Mark where platelets are.
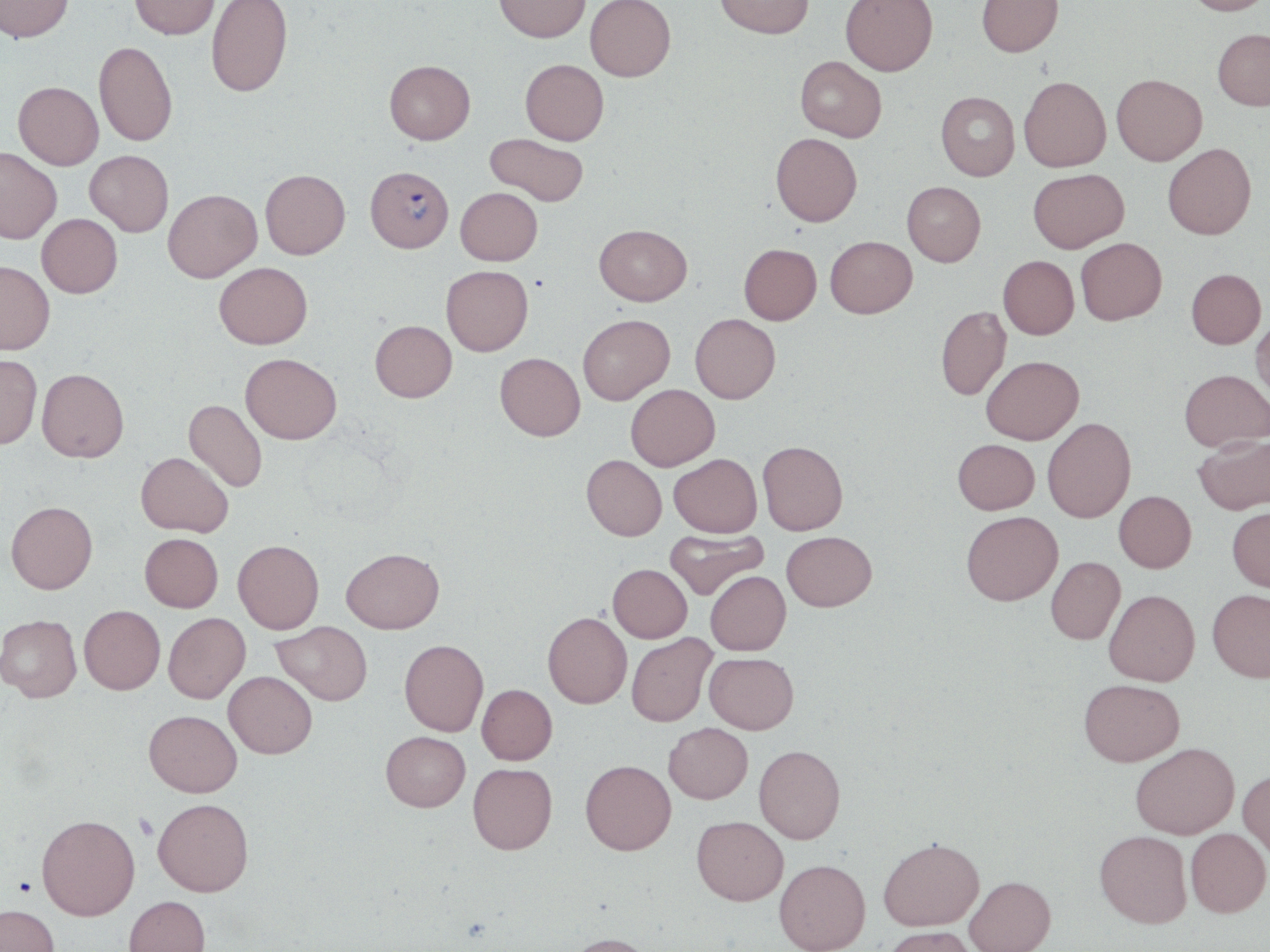

Approximate bounding boxes as (x1,y1)-(x2,y2) corner pairs in pixels.
Platelets: (134,814)-(158,840), (13,876)-(36,896).

Plasmodium falciparum-infected red blood cell locations: (365,166)-(453,252). Uninfected red blood cell locations: (0,0)-(74,42), (129,0)-(220,39), (206,0)-(293,97), (494,0)-(590,42), (585,0)-(676,82), (715,0)-(814,38), (840,0)-(938,76), (976,0)-(1063,56), (1183,0)-(1270,15), (1213,28)-(1270,110), (94,41)-(177,146), (795,56)-(887,142), (520,59)-(609,145), (384,60)-(475,144), (1112,73)-(1207,165), (1019,76)-(1111,172), (13,81)-(103,170), (936,91)-(1019,181), (771,132)-(862,226), (485,133)-(589,206), (1163,143)-(1256,239), (0,147)-(62,244), (84,150)-(173,237), (1028,168)-(1129,252), (260,169)-(350,259), (902,181)-(986,266), (455,187)-(542,265), (163,189)-(262,282), (37,214)-(122,298), (594,224)-(692,305), (825,236)-(916,317), (1075,237)-(1167,325), (739,243)-(821,325), (998,255)-(1079,339), (0,260)-(54,354), (214,262)-(312,348), (441,265)-(533,356), (1186,268)-(1265,348), (936,305)-(1011,401), (578,314)-(674,404), (690,314)-(780,403), (1251,315)-(1270,406), (370,320)-(457,402), (0,353)-(42,449), (241,353)-(341,444), (495,353)-(585,440), (981,356)-(1084,444), (37,368)-(129,462), (1179,369)-(1269,452), (626,384)-(719,470), (184,399)-(268,492), (1042,417)-(1136,523), (1193,434)-(1270,515), (953,438)-(1039,514), (758,441)-(848,535), (136,452)-(233,536), (669,453)-(762,537), (581,455)-(667,540), (1114,490)-(1196,572), (6,500)-(98,593), (1227,506)-(1270,592), (961,510)-(1063,605), (664,529)-(768,600), (782,531)-(877,611), (140,533)-(223,612), (233,539)-(324,633), (341,547)-(444,633), (1046,556)-(1125,644), (608,564)-(692,642), (705,570)-(791,655), (1104,589)-(1200,686), (1207,589)-(1270,682), (79,605)-(165,694), (163,612)-(250,702), (543,612)-(632,708), (0,614)-(81,702), (273,620)-(372,705), (627,633)-(716,726), (400,639)-(488,736), (704,652)-(799,734), (224,671)-(317,758), (1079,678)-(1184,765), (477,684)-(557,764), (144,710)-(242,796), (664,722)-(753,803), (381,731)-(470,811), (1130,742)-(1239,839), (754,744)-(845,844), (580,759)-(676,855), (468,762)-(557,854), (1238,769)-(1270,858), (153,798)-(253,896), (37,814)-(140,920), (692,815)-(788,905), (1185,828)-(1270,917), (1094,830)-(1192,928), (878,837)-(984,930), (774,859)-(870,952), (964,875)-(1055,952), (123,895)-(210,952), (0,904)-(59,952), (880,926)-(979,952), (562,932)-(658,952). Slide-level diagnosis: Plasmodium falciparum. Light microscopy. Captured at 1000x magnification. Image is 1270×952 pixels. May-Grünwald-Giemsa stain. Thin blood smear. One field of a larger specimen.